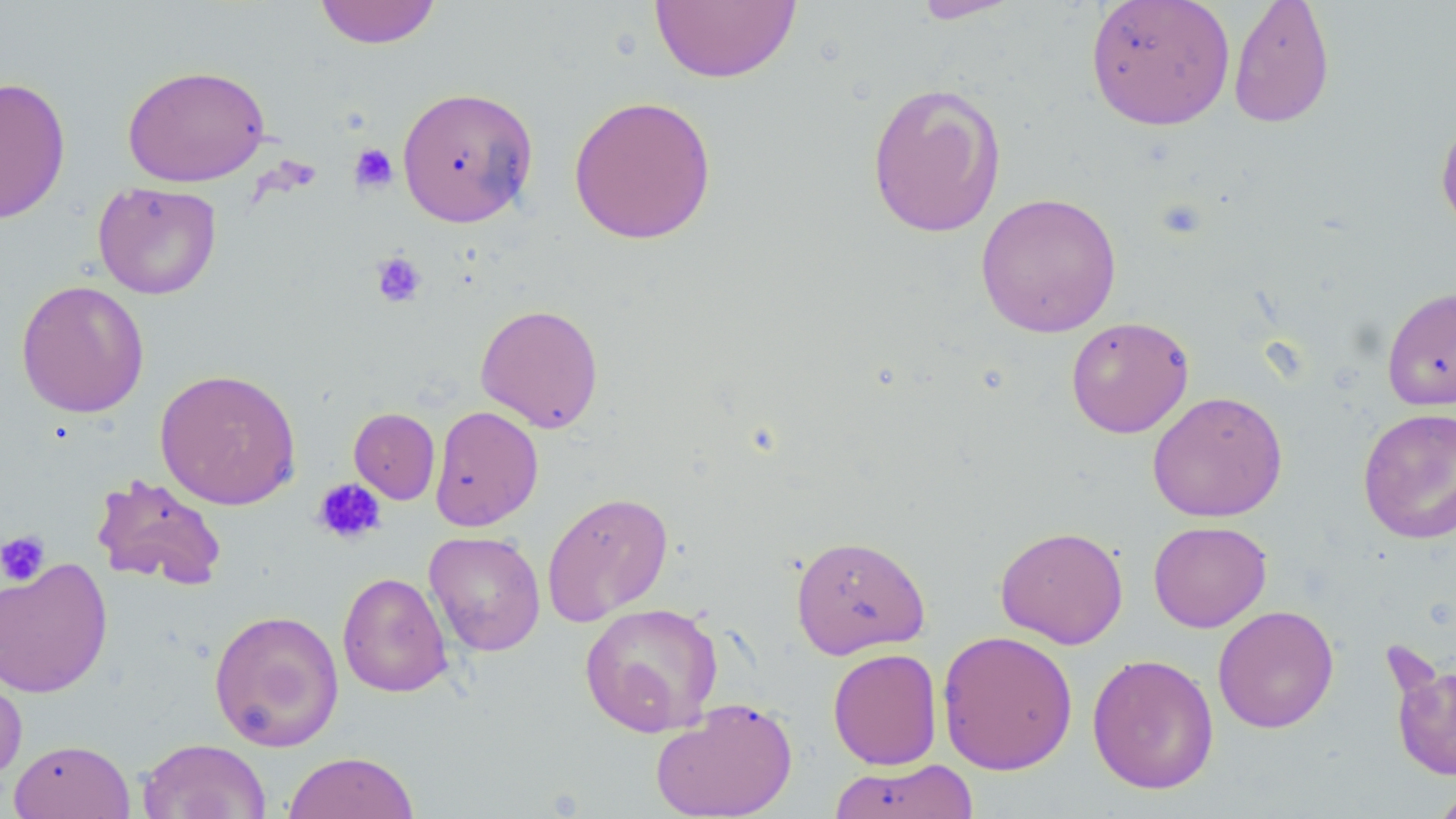 Approximate bounding boxes as [x1, y1, x2, y2] in pixels. Platelet locations: [348, 143, 398, 194], [1157, 198, 1206, 239], [371, 251, 427, 307], [313, 478, 386, 544], [0, 530, 51, 586]. Uninfected red blood cell locations: [314, 0, 441, 49], [650, 0, 801, 84], [910, 0, 1024, 24], [1085, 0, 1236, 130], [1228, 0, 1335, 128], [122, 64, 270, 187], [0, 76, 71, 225], [866, 82, 1007, 238], [396, 86, 539, 228], [568, 95, 717, 245], [1435, 114, 1456, 237], [93, 181, 222, 299], [975, 192, 1122, 338], [16, 279, 149, 418], [1381, 286, 1456, 411], [475, 303, 604, 433], [1066, 316, 1194, 438], [154, 368, 302, 510], [1147, 390, 1288, 523], [429, 405, 543, 532], [1357, 406, 1456, 545], [349, 407, 440, 504], [91, 473, 228, 591], [541, 491, 674, 626], [1148, 520, 1272, 632], [995, 525, 1129, 649], [424, 530, 546, 656], [790, 534, 929, 659], [0, 557, 113, 699], [337, 571, 452, 698], [579, 602, 723, 738], [1213, 605, 1339, 733], [208, 609, 345, 751], [937, 630, 1078, 775], [827, 648, 943, 770], [1087, 653, 1219, 795], [1390, 655, 1455, 782], [0, 662, 27, 786], [649, 697, 798, 819], [137, 738, 271, 819], [9, 739, 135, 819], [282, 751, 420, 819], [828, 758, 979, 819], [1431, 787, 1456, 818]. Slide-level diagnosis: no evidence of blood parasites. Light microscopy. Single field of view. 1000x magnification. Image is 1456×819 pixels. Thin blood smear. May-Grünwald-Giemsa stain.